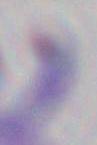
identification: Toxoplasma gondii
magnification: 1000x
modality: micrograph